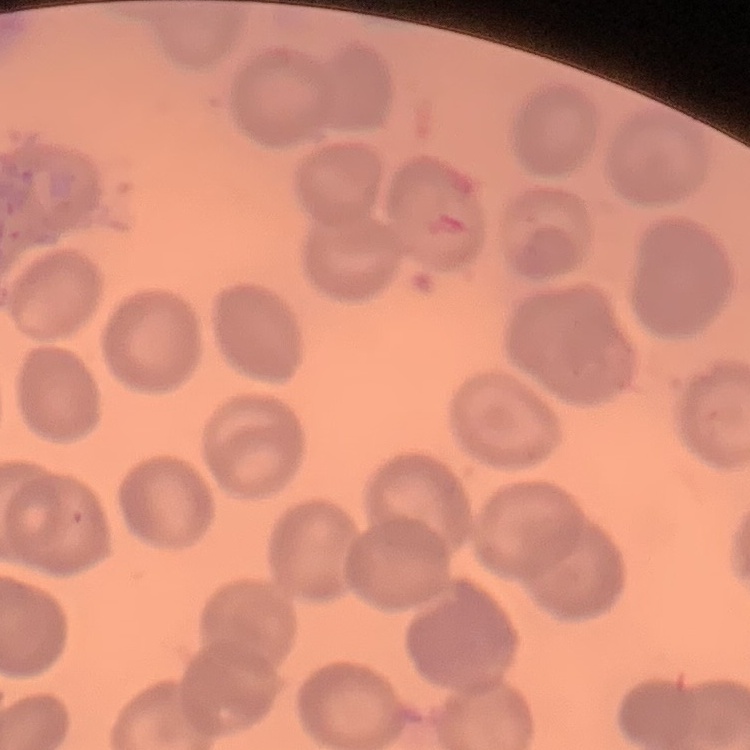
The erythrocytes exhibit no rouleaux formation. Stained with either Field's or Giemsa. Thin blood film. One tile cut from a larger photomicrograph.